Assess this cell for malaria.
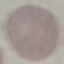

It is uninfected.

Summary:
  - Image type: automatically extracted cell patch, resized to 64 × 64 pixels
  - Preparation: thin blood smear
  - Capture: smartphone camera at the microscope eyepiece
  - Stain: Giemsa